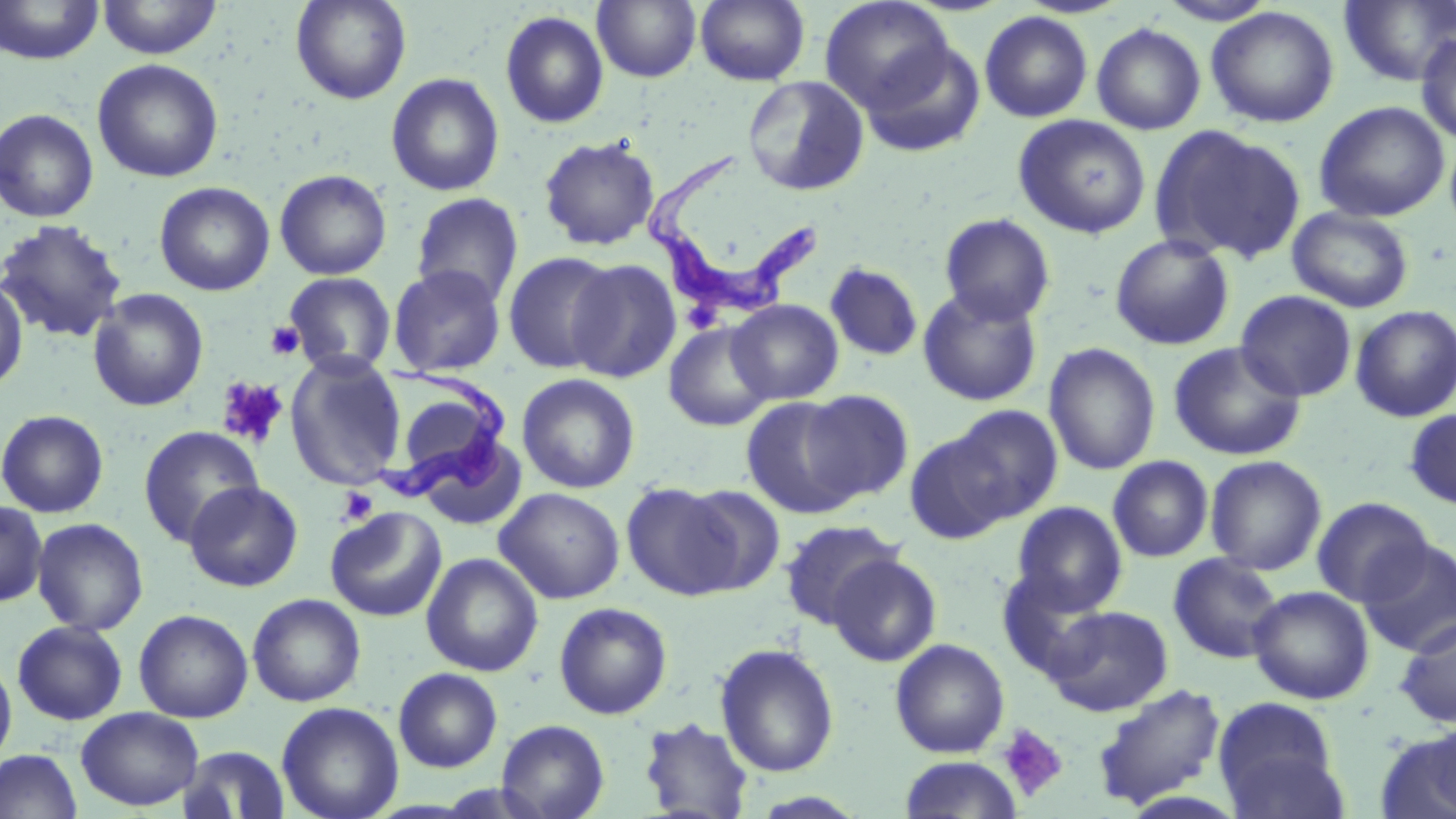

{
  "slide_level_diagnosis": "Trypanosoma brucei",
  "magnification": "1000x",
  "preparation": "thin blood film",
  "image_size": "1456×819 pixels",
  "stain": "May-Grünwald-Giemsa",
  "trypanosoma_brucei_locations": "approximate bounding boxes as named x1/y1/x2/y2 corners in pixels: (x1=644, y1=147, x2=814, y2=321), (x1=369, y1=368, x2=511, y2=502)",
  "field_of_view": "single",
  "platelet_locations": "approximate bounding boxes as named x1/y1/x2/y2 corners in pixels: (x1=265, y1=320, x2=305, y2=360), (x1=217, y1=377, x2=288, y2=449), (x1=337, y1=487, x2=378, y2=526), (x1=997, y1=723, x2=1069, y2=802)",
  "modality": "optical microscopy",
  "uninfected_red_blood_cell_locations": "approximate bounding boxes as named x1/y1/x2/y2 corners in pixels: (x1=96, y1=0, x2=223, y2=60), (x1=291, y1=0, x2=412, y2=104), (x1=592, y1=0, x2=701, y2=83), (x1=694, y1=0, x2=810, y2=86), (x1=1338, y1=0, x2=1456, y2=87), (x1=1, y1=1, x2=104, y2=66), (x1=820, y1=1, x2=955, y2=113), (x1=1205, y1=6, x2=1340, y2=128), (x1=500, y1=10, x2=609, y2=128), (x1=979, y1=11, x2=1093, y2=123), (x1=1091, y1=22, x2=1206, y2=135), (x1=1416, y1=31, x2=1456, y2=147), (x1=859, y1=38, x2=986, y2=159), (x1=92, y1=58, x2=224, y2=183), (x1=386, y1=72, x2=504, y2=196), (x1=742, y1=75, x2=870, y2=197), (x1=1313, y1=101, x2=1450, y2=223), (x1=0, y1=108, x2=99, y2=223), (x1=1013, y1=114, x2=1151, y2=239), (x1=1151, y1=125, x2=1306, y2=265), (x1=538, y1=135, x2=660, y2=251), (x1=274, y1=169, x2=392, y2=280), (x1=154, y1=181, x2=275, y2=296), (x1=411, y1=192, x2=525, y2=308), (x1=1287, y1=206, x2=1414, y2=313), (x1=939, y1=213, x2=1056, y2=326), (x1=0, y1=219, x2=128, y2=344), (x1=1110, y1=234, x2=1235, y2=350), (x1=503, y1=251, x2=619, y2=374), (x1=567, y1=259, x2=682, y2=383), (x1=824, y1=262, x2=923, y2=361), (x1=388, y1=264, x2=506, y2=377), (x1=284, y1=272, x2=397, y2=376), (x1=0, y1=275, x2=29, y2=394), (x1=917, y1=287, x2=1043, y2=406), (x1=88, y1=288, x2=209, y2=412), (x1=1235, y1=290, x2=1357, y2=402), (x1=726, y1=299, x2=844, y2=404), (x1=1350, y1=305, x2=1456, y2=423), (x1=663, y1=321, x2=775, y2=432), (x1=1167, y1=341, x2=1307, y2=461), (x1=1044, y1=342, x2=1161, y2=476), (x1=284, y1=354, x2=407, y2=490), (x1=516, y1=373, x2=640, y2=494), (x1=802, y1=390, x2=914, y2=501), (x1=740, y1=396, x2=864, y2=519), (x1=944, y1=405, x2=1064, y2=523), (x1=1404, y1=407, x2=1456, y2=509), (x1=0, y1=409, x2=109, y2=518), (x1=138, y1=425, x2=263, y2=547), (x1=903, y1=429, x2=1014, y2=544), (x1=415, y1=437, x2=528, y2=531), (x1=1107, y1=455, x2=1214, y2=562), (x1=1205, y1=455, x2=1327, y2=575), (x1=184, y1=481, x2=303, y2=592), (x1=621, y1=482, x2=742, y2=600), (x1=678, y1=484, x2=786, y2=595), (x1=494, y1=487, x2=625, y2=604), (x1=1311, y1=497, x2=1433, y2=606), (x1=0, y1=499, x2=48, y2=609), (x1=1011, y1=501, x2=1128, y2=616), (x1=325, y1=507, x2=448, y2=622), (x1=31, y1=517, x2=149, y2=635), (x1=780, y1=519, x2=906, y2=629), (x1=1358, y1=538, x2=1456, y2=657), (x1=421, y1=553, x2=544, y2=676), (x1=1168, y1=553, x2=1284, y2=664), (x1=826, y1=554, x2=941, y2=667), (x1=997, y1=568, x2=1111, y2=681), (x1=1248, y1=586, x2=1375, y2=704), (x1=247, y1=593, x2=366, y2=706), (x1=553, y1=602, x2=673, y2=719), (x1=1045, y1=604, x2=1173, y2=716), (x1=134, y1=609, x2=254, y2=723), (x1=1394, y1=616, x2=1456, y2=728), (x1=12, y1=620, x2=128, y2=726), (x1=889, y1=638, x2=1010, y2=758), (x1=714, y1=643, x2=840, y2=778), (x1=0, y1=651, x2=17, y2=771), (x1=393, y1=668, x2=503, y2=772), (x1=1091, y1=682, x2=1227, y2=811), (x1=1213, y1=696, x2=1344, y2=817), (x1=276, y1=701, x2=404, y2=819), (x1=76, y1=707, x2=203, y2=811), (x1=638, y1=716, x2=754, y2=818), (x1=496, y1=719, x2=609, y2=819), (x1=1376, y1=729, x2=1456, y2=819), (x1=177, y1=745, x2=291, y2=818), (x1=0, y1=748, x2=82, y2=819), (x1=897, y1=756, x2=1023, y2=819)"
}